Comment on the morphology of the erythrocytes.
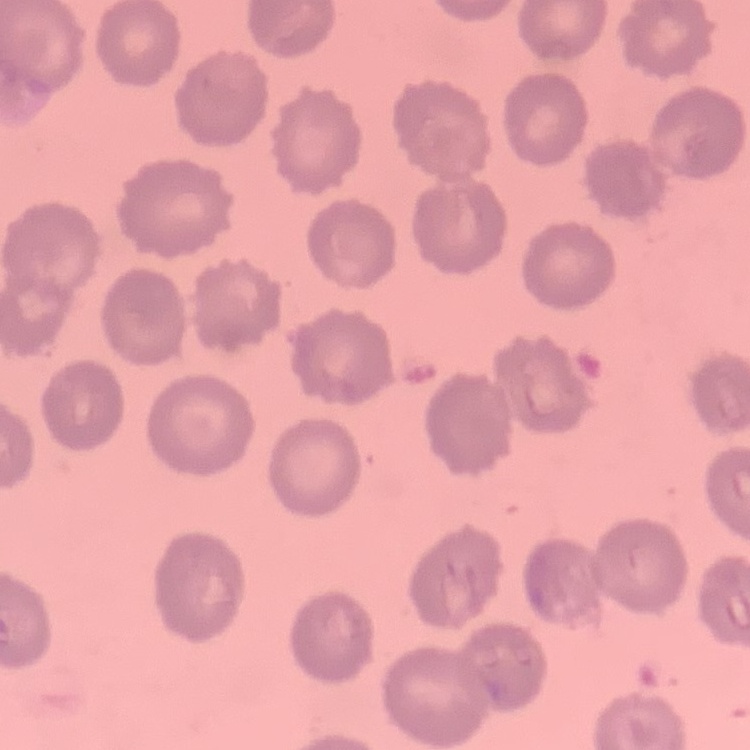

They show no rouleaux formation.

{
  "image_type": "square crop of a larger photomicrograph",
  "stain": "Field's or Giemsa",
  "preparation": "thin blood smear"
}